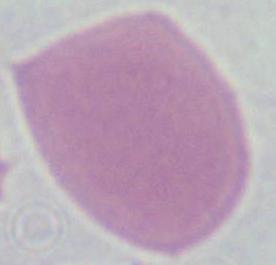

A red blood cell is seen. Micrograph. 1000x magnification.